Report the malaria status of this cell.
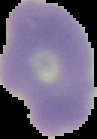
Uninfected.

From a thin blood film. The area outside the segmented cell region is set to black. Image is 97×139 pixels.